Name the parasite shown.
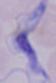

This is a trypanosome.

magnification = 1000x
modality = micrograph